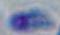

1000x magnification. Toxoplasma gondii is shown. Photomicrograph.